Locate and identify every blood parasite.
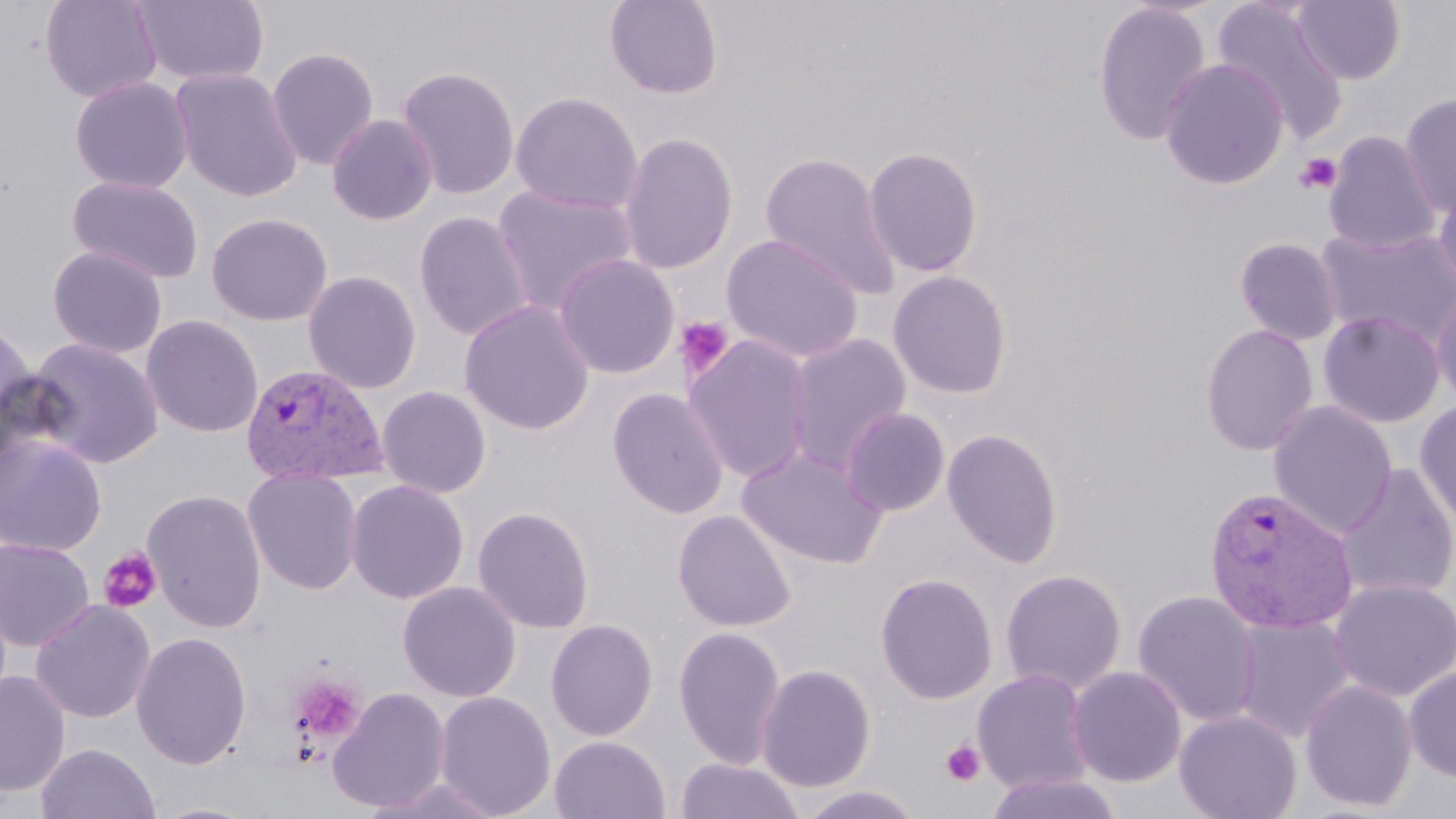
Approximate bounding boxes as [x1, y1, x2, y2] in pixels.
Plasmodium vivax-infected red blood cells: [239, 363, 388, 486], [1204, 486, 1358, 636].
No Plasmodium falciparum, Plasmodium ovale, Plasmodium malariae, Babesia divergens, or Trypanosoma brucei observed.

slide-level diagnosis = Plasmodium vivax
preparation = thin blood smear
stain = May-Grünwald-Giemsa
modality = light microscopy
uninfected red blood cell locations = approximate bounding boxes as [x1, y1, x2, y2] in pixels: [40, 0, 162, 103], [604, 0, 724, 99], [1211, 0, 1348, 142], [133, 1, 269, 86], [1291, 1, 1407, 85], [1092, 2, 1212, 147], [266, 47, 379, 170], [1159, 58, 1289, 189], [395, 66, 520, 201], [170, 67, 304, 202], [69, 76, 193, 193], [510, 92, 643, 215], [1398, 94, 1456, 216], [326, 114, 437, 225], [618, 131, 738, 274], [1323, 131, 1441, 256], [863, 146, 984, 277], [760, 151, 902, 299], [68, 175, 205, 284], [1434, 179, 1456, 297], [492, 186, 637, 315], [414, 212, 533, 342], [206, 213, 333, 326], [1315, 226, 1456, 348], [721, 234, 865, 364], [1234, 237, 1342, 346], [47, 246, 167, 359], [553, 254, 680, 379], [303, 270, 422, 394], [887, 270, 1013, 399], [1430, 286, 1456, 409], [459, 300, 595, 436], [1318, 310, 1445, 428], [141, 315, 264, 437], [0, 317, 38, 449], [1200, 323, 1319, 456], [785, 333, 911, 473], [683, 335, 812, 484], [25, 338, 164, 469], [377, 385, 491, 498], [607, 387, 728, 519], [1414, 399, 1456, 532], [1267, 401, 1397, 539], [840, 407, 950, 517], [942, 427, 1064, 569], [0, 435, 107, 557], [738, 447, 887, 569], [1334, 464, 1456, 603], [242, 468, 363, 595], [345, 479, 470, 605], [142, 489, 267, 633], [472, 505, 595, 634], [672, 509, 796, 632], [0, 536, 95, 652], [1000, 569, 1127, 694], [874, 572, 998, 705], [1328, 578, 1456, 701], [397, 581, 522, 702], [1132, 590, 1262, 728], [30, 599, 155, 724], [1231, 617, 1354, 744], [545, 619, 659, 741], [673, 625, 787, 770], [131, 631, 252, 770], [756, 663, 877, 793], [1403, 665, 1456, 782], [1067, 666, 1186, 788], [972, 669, 1094, 794], [0, 670, 71, 798], [1300, 680, 1418, 812], [327, 687, 451, 812], [434, 691, 556, 818], [1174, 711, 1302, 819], [549, 735, 670, 819], [35, 742, 161, 819], [675, 757, 802, 819], [982, 771, 1124, 819], [360, 776, 504, 819], [795, 785, 927, 819], [146, 800, 266, 819]
field of view = single
image size = 1456×819 pixels
magnification = 1000x
platelet locations = approximate bounding boxes as [x1, y1, x2, y2] in pixels: [1294, 152, 1342, 194], [674, 315, 734, 379], [98, 547, 162, 614], [287, 673, 367, 747], [940, 739, 987, 787]